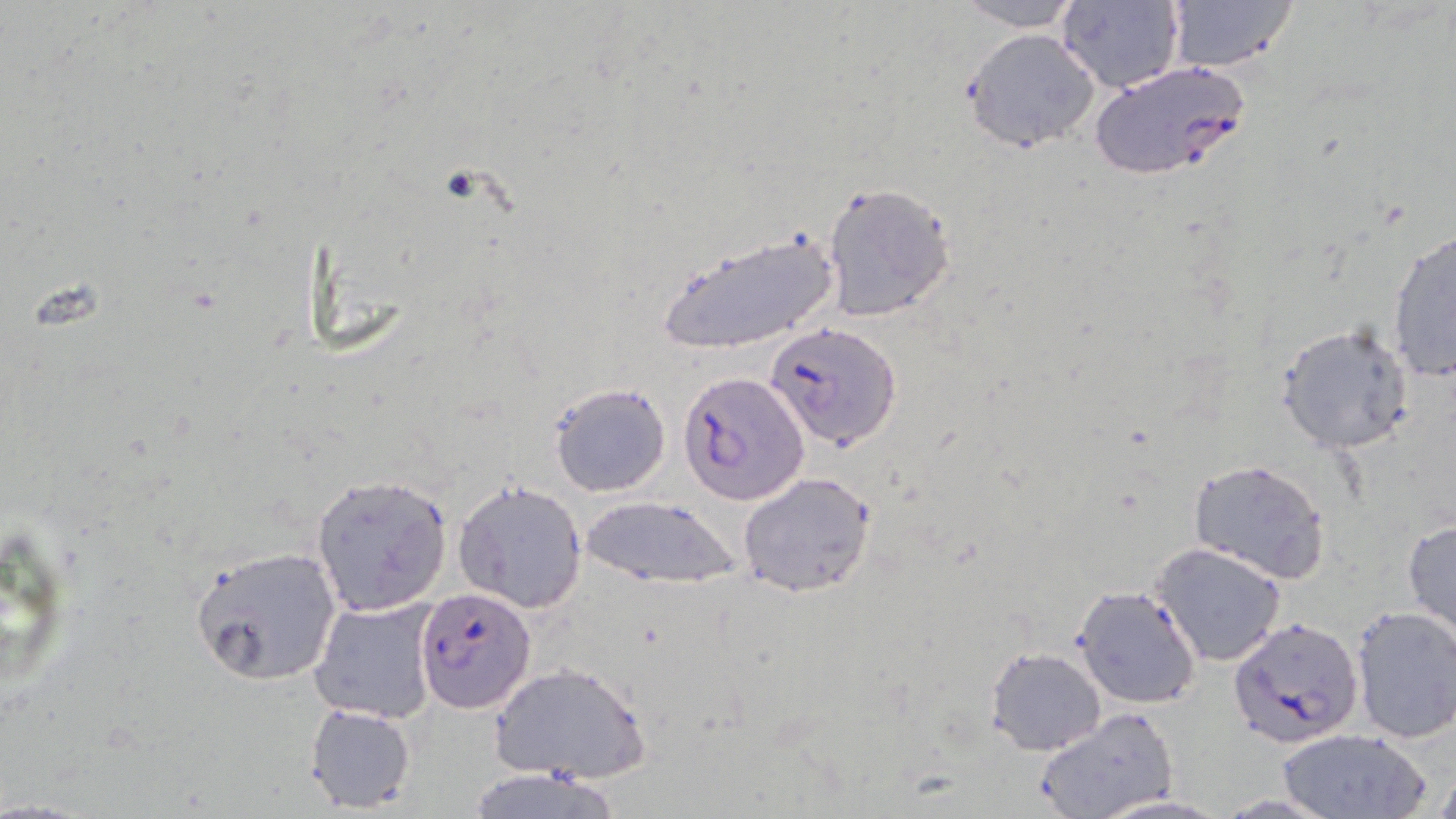

Summary:
  - Coordinate format: approximate bounding boxes as named x1/y1/x2/y2 corners in pixels
  - Uninfected red blood cell locations: (x1=953, y1=0, x2=1084, y2=31), (x1=1161, y1=0, x2=1303, y2=73), (x1=1055, y1=1, x2=1184, y2=94), (x1=961, y1=28, x2=1100, y2=152), (x1=820, y1=182, x2=957, y2=324), (x1=1385, y1=226, x2=1455, y2=385), (x1=655, y1=230, x2=842, y2=357), (x1=1275, y1=321, x2=1414, y2=455), (x1=549, y1=382, x2=671, y2=498), (x1=1188, y1=458, x2=1332, y2=583), (x1=738, y1=471, x2=877, y2=598), (x1=309, y1=472, x2=452, y2=616), (x1=454, y1=480, x2=588, y2=612), (x1=580, y1=496, x2=741, y2=590), (x1=1402, y1=517, x2=1456, y2=644), (x1=0, y1=521, x2=83, y2=698), (x1=1153, y1=541, x2=1288, y2=667), (x1=190, y1=544, x2=344, y2=687), (x1=1072, y1=585, x2=1201, y2=710), (x1=308, y1=597, x2=442, y2=723), (x1=1349, y1=603, x2=1456, y2=745), (x1=986, y1=646, x2=1106, y2=755), (x1=491, y1=661, x2=651, y2=785), (x1=303, y1=703, x2=416, y2=814), (x1=1036, y1=707, x2=1177, y2=819), (x1=1276, y1=728, x2=1429, y2=819), (x1=1426, y1=756, x2=1456, y2=819), (x1=459, y1=767, x2=625, y2=819), (x1=1090, y1=793, x2=1231, y2=817)
  - Plasmodium falciparum-infected red blood cell locations: (x1=1088, y1=60, x2=1249, y2=182), (x1=766, y1=320, x2=902, y2=451), (x1=677, y1=371, x2=808, y2=505), (x1=415, y1=588, x2=536, y2=712), (x1=1229, y1=616, x2=1363, y2=748)
  - Slide-level diagnosis: Plasmodium falciparum
  - Modality: light microscopy
  - Field of view: one of a larger specimen
  - Preparation: thin blood smear
  - Image size: 1456×819 pixels
  - Stain: May-Grünwald-Giemsa
  - Magnification: 1000x